Report the malaria status of this cell.
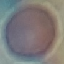

Uninfected.

{
  "image_type": "cell patch, automatically extracted from a larger field of view and resized to 64 × 64 pixels",
  "stain": "Giemsa",
  "preparation": "thin blood smear",
  "capture": "smartphone through the microscope eyepiece"
}